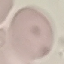

{
  "result": "no malaria parasites detected",
  "capture": "smartphone camera at the microscope eyepiece",
  "stain": "Giemsa",
  "image_type": "automatically extracted cell patch, resized to 64 × 64 pixels",
  "preparation": "thin blood smear"
}